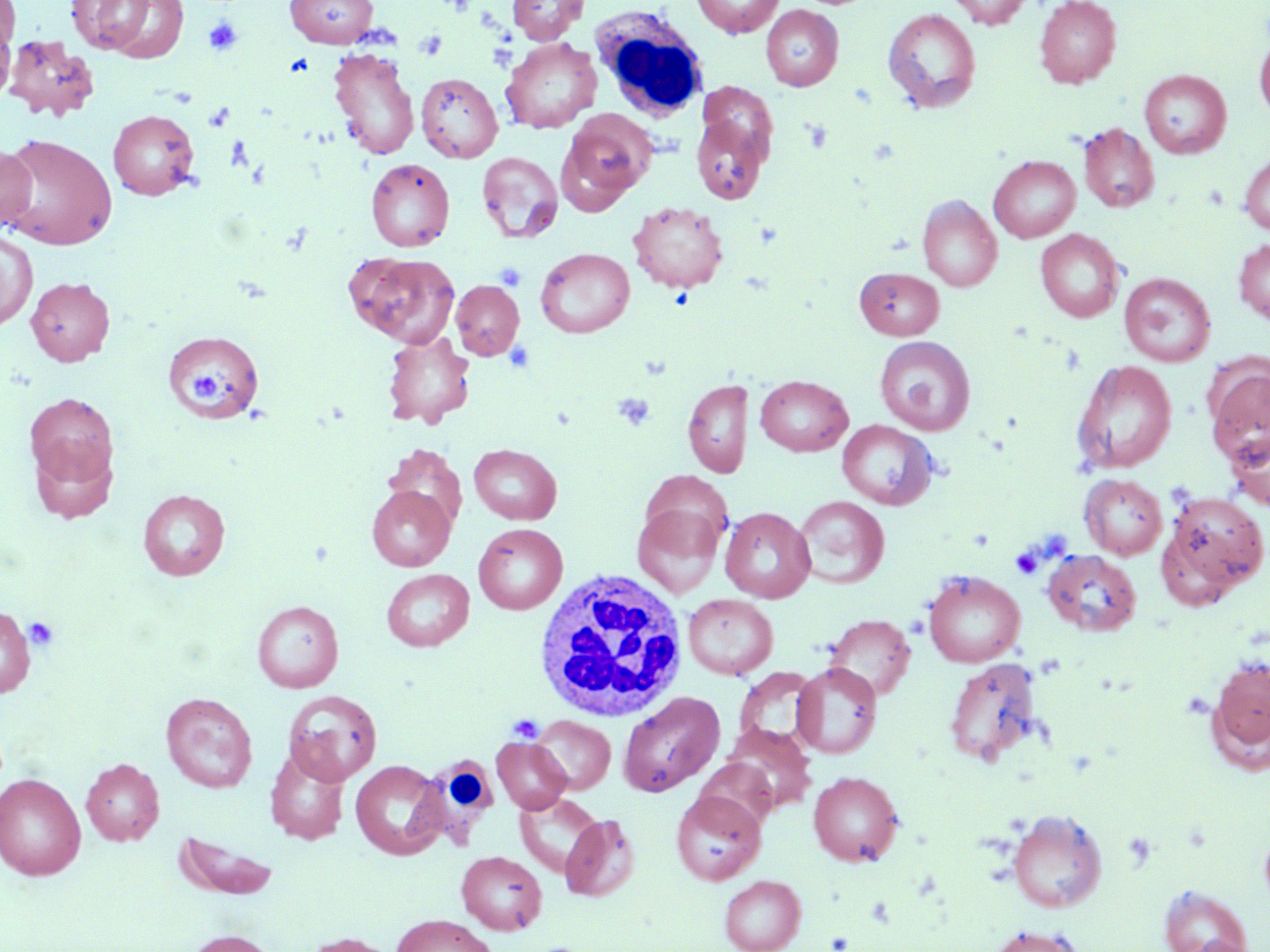

Summary:
  - Coordinate format: approximate bounding boxes as (x1,y1)-(x2,y2) corner pairs in pixels
  - Uninfected red blood cell locations: (66,0)-(187,60), (284,0)-(379,47), (508,0)-(588,44), (692,0)-(784,37), (947,0)-(1032,29), (1035,0)-(1122,88), (0,1)-(19,60), (761,5)-(843,90), (882,8)-(982,113), (0,11)-(16,108), (1254,33)-(1270,121), (3,36)-(99,121), (501,37)-(601,133), (328,47)-(420,161), (1139,70)-(1231,159), (416,72)-(502,162), (698,86)-(777,177), (108,109)-(199,200), (558,112)-(655,211), (691,116)-(768,204), (1078,123)-(1159,214), (0,133)-(118,250), (0,143)-(37,231), (1239,150)-(1270,236), (476,152)-(563,243), (989,155)-(1081,242), (366,158)-(454,251), (918,195)-(1002,292), (629,201)-(729,293), (1035,229)-(1124,322), (0,231)-(37,331), (1233,238)-(1270,325), (536,248)-(635,337), (346,252)-(459,348), (854,267)-(944,339), (1119,273)-(1216,367), (26,276)-(115,366), (451,280)-(524,360), (163,330)-(264,421), (383,331)-(475,429), (874,336)-(975,435), (1072,359)-(1178,474), (1204,361)-(1270,467), (755,375)-(852,456), (683,379)-(752,478), (24,392)-(118,493), (837,420)-(937,509), (1225,426)-(1270,511), (28,434)-(116,525), (383,444)-(466,531), (469,444)-(562,525), (1079,474)-(1167,560), (367,485)-(455,571), (138,489)-(230,581), (1160,489)-(1269,601), (794,495)-(889,589), (633,505)-(723,599), (720,507)-(815,603), (474,523)-(567,614), (1043,549)-(1142,637), (381,569)-(474,651), (923,570)-(1025,668), (683,593)-(778,680), (252,600)-(343,692), (0,607)-(36,697), (824,613)-(915,703), (1207,653)-(1270,768), (944,657)-(1043,767), (791,662)-(882,759), (734,667)-(819,751), (283,690)-(382,786), (161,692)-(257,793), (619,692)-(724,796), (532,716)-(615,794), (723,724)-(816,814), (492,737)-(571,814), (265,748)-(350,845), (81,758)-(165,845), (695,759)-(778,831), (350,760)-(448,860), (808,771)-(903,866), (0,773)-(86,880), (671,791)-(765,884), (514,792)-(606,878), (1006,809)-(1107,912), (560,813)-(640,901), (1259,824)-(1270,912), (175,831)-(280,900), (456,851)-(546,934), (719,875)-(806,952), (1157,883)-(1253,952), (392,914)-(496,952), (986,924)-(1085,952), (182,929)-(280,952), (301,932)-(400,952), (1184,937)-(1257,952)
  - White blood cell locations: (590,6)-(710,121), (532,566)-(689,724), (406,748)-(506,851)
  - Platelet locations: (203,17)-(244,56), (414,30)-(448,60), (204,102)-(234,132), (494,263)-(526,291), (186,367)-(223,405), (612,392)-(655,431), (1010,546)-(1043,580), (23,616)-(59,651), (508,714)-(544,742)
  - Slide-level diagnosis: no evidence of blood parasites
  - Stain: May-Grünwald-Giemsa
  - Magnification: 1000x
  - Modality: light microscopy
  - Preparation: thin blood film
  - Field of view: one of a larger specimen
  - Image size: 1270×952 pixels